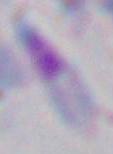

Captured at 1000x magnification. Micrograph. Toxoplasma gondii is seen.